Assess this cell for malaria.
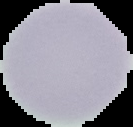
Uninfected.

image size = 133×127 pixels
image type = segmented cell region on a black background
preparation = thin blood film